Identify the cell.
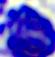
A leukocyte.

Captured at 400x magnification. Photomicrograph.